Describe the morphology of the erythrocytes.
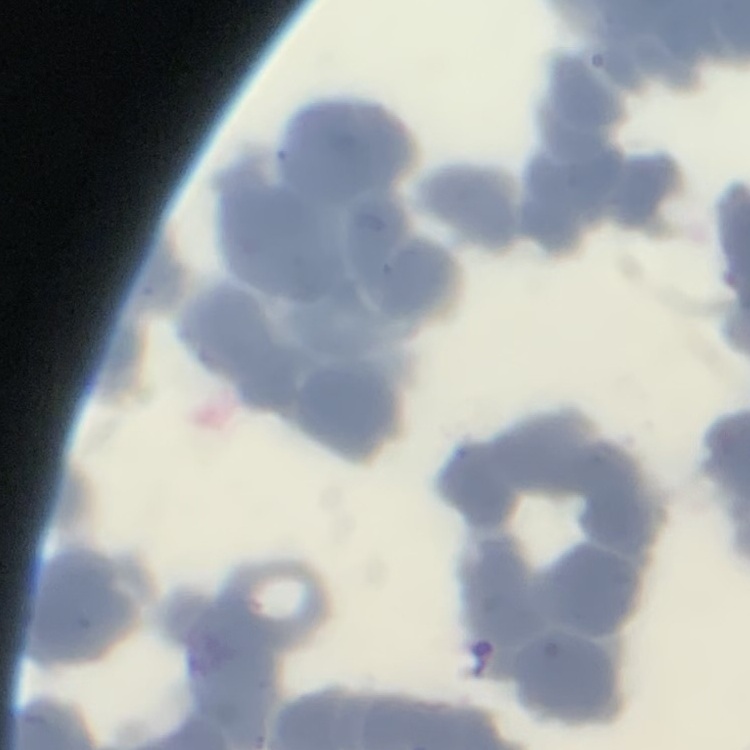

They show rouleaux formation.

stain = Field's or Giemsa
preparation = thin blood smear
image type = square crop of a larger photomicrograph